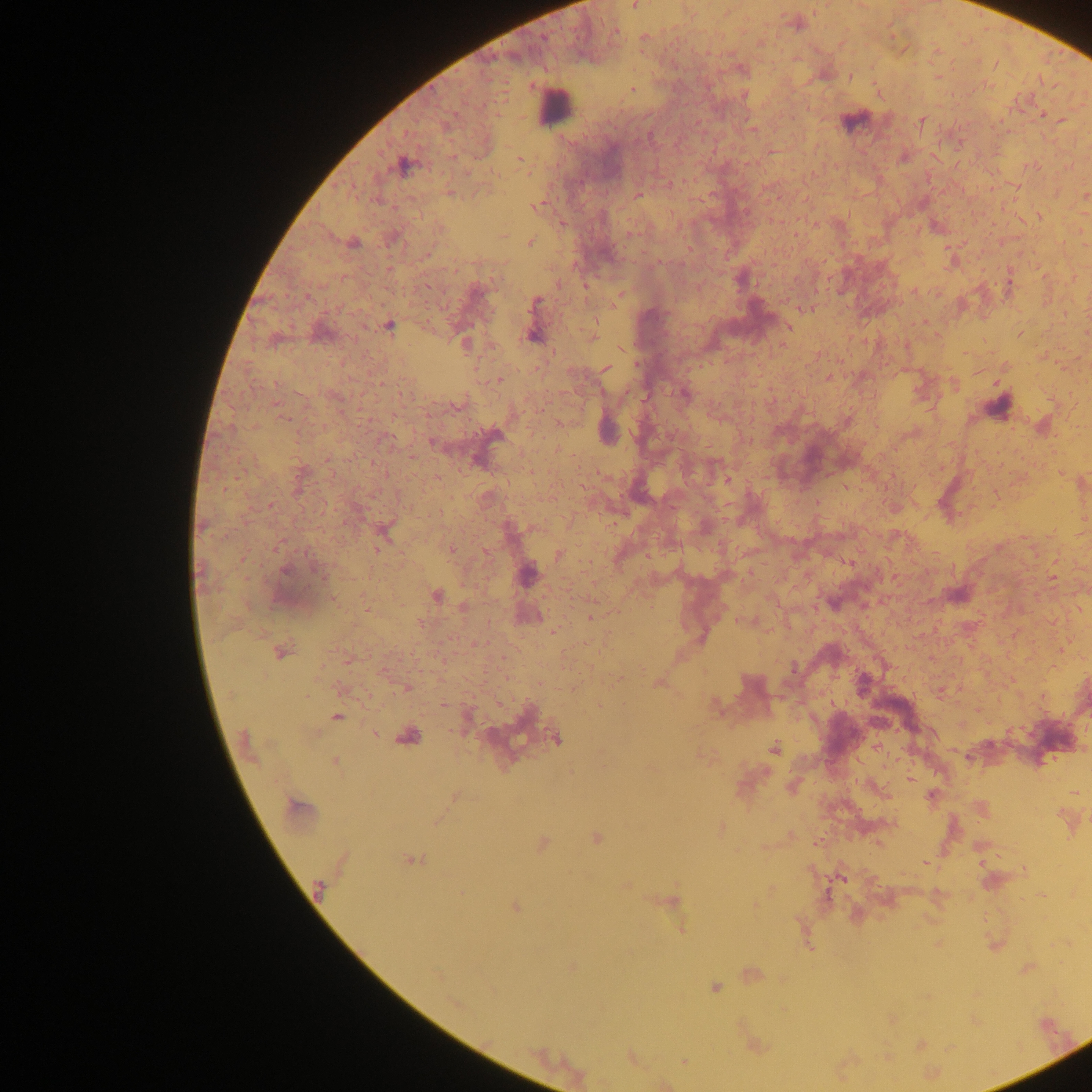
Approximate centers as [x, y] in pixels.
Summary:
  - Malaria parasite locations: [635, 6], [815, 8], [726, 12], [796, 23], [615, 31], [644, 37], [994, 64], [937, 76], [849, 77], [632, 89], [879, 92], [744, 94], [1042, 114], [922, 120], [1061, 120], [752, 129], [934, 156], [520, 160], [404, 166], [1032, 166], [669, 184], [1016, 186], [1085, 195], [638, 196], [538, 205], [1039, 215], [815, 223], [795, 235], [529, 241], [352, 242], [1084, 244], [952, 261], [558, 282], [914, 291], [619, 297], [806, 307], [1065, 312], [923, 321], [533, 322], [388, 325], [788, 326], [1086, 331], [1019, 333], [592, 337], [465, 344], [621, 348], [1061, 364], [605, 368], [827, 377], [498, 380], [997, 382], [954, 384], [684, 394], [1042, 426], [606, 428], [1061, 473], [726, 480], [1082, 482], [1084, 519], [384, 531], [450, 549], [485, 551], [559, 554], [527, 573], [1053, 577], [435, 595], [957, 595], [464, 606], [367, 609], [1080, 609], [528, 616], [591, 617], [744, 621], [554, 631], [1060, 648], [280, 651], [347, 660], [658, 683], [406, 687], [340, 688], [940, 691], [444, 704], [599, 706], [715, 706], [978, 709], [336, 716], [375, 733], [408, 736], [556, 738], [245, 744], [774, 748], [334, 762], [910, 780], [791, 786], [1075, 792], [455, 796], [932, 796], [298, 808], [981, 809], [720, 828], [789, 835], [596, 837], [816, 842], [542, 844], [412, 860], [925, 863], [980, 863], [842, 877], [626, 885], [318, 889], [1041, 895], [670, 901], [754, 905], [515, 907], [680, 928], [571, 965], [1027, 968], [750, 974], [714, 987], [890, 1019], [920, 1044], [754, 1046], [540, 1054], [631, 1057], [684, 1060], [665, 1084]
  - Leukocyte locations: [554, 106], [857, 120], [998, 407]
  - Field of view: single
  - Capture: mobile-phone photograph through a microscope
  - Preparation: thick blood smear
  - Image size: 1092×1092 pixels
  - Country: Ghana